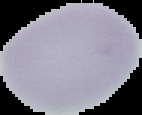
image type = cell region segmented out of the field of view; surrounding area masked to black
image size = 142×115 pixels
preparation = thin blood smear
result = negative for Plasmodium parasites